Look for Plasmodium parasites.
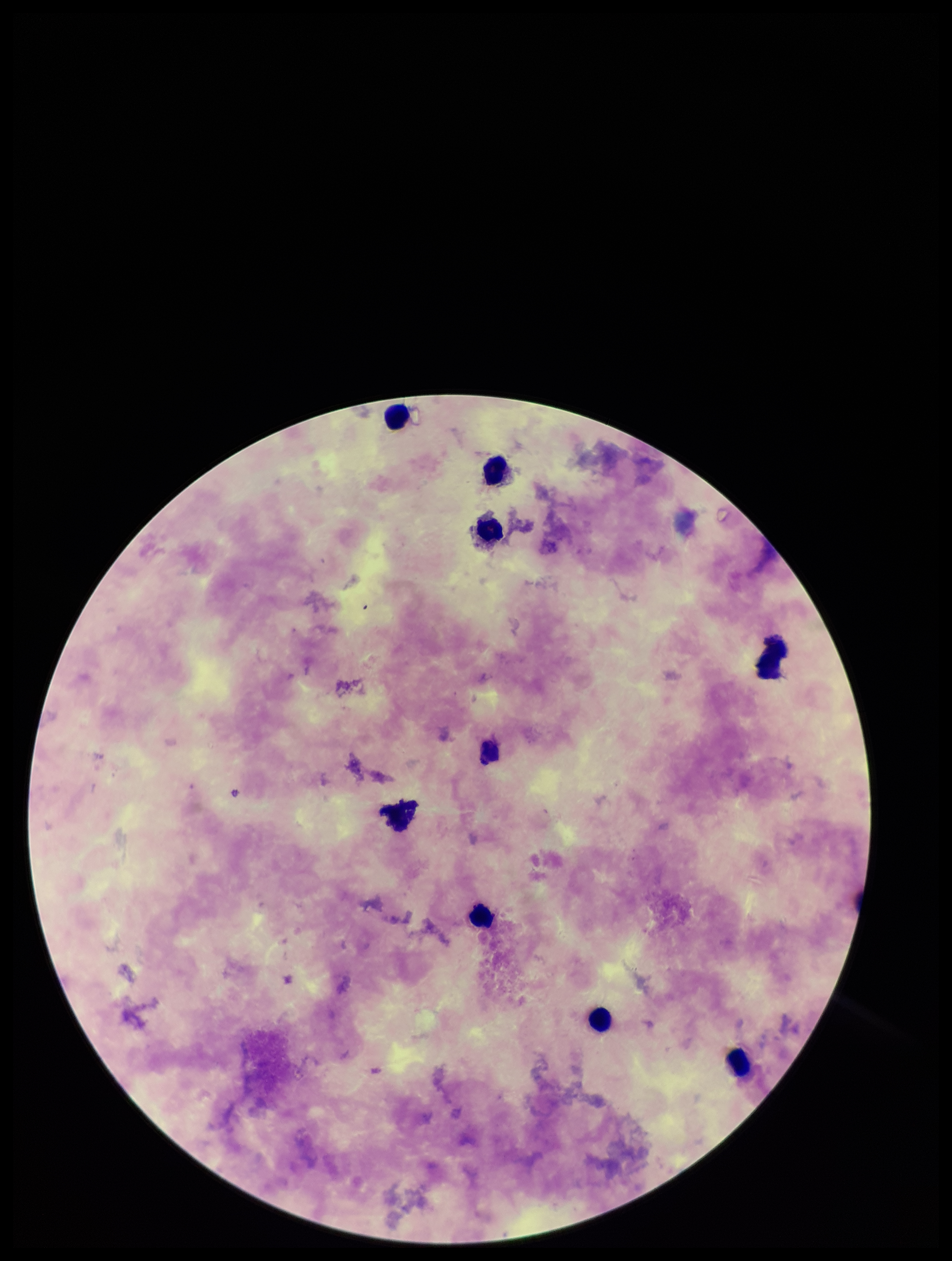
None identified.

Preparation: thick. Image is 952×1261 pixels. Patient malaria status: negative. Giemsa stain. Leukocyte count: 8. Parasite count: 0. Photographed through the microscope eyepiece with a smartphone camera. One field from this slide.